Report the malaria status of this cell.
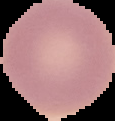

It is uninfected.

Image is 115×121 pixels. The area outside the segmented cell region is set to black. From a thin blood smear.